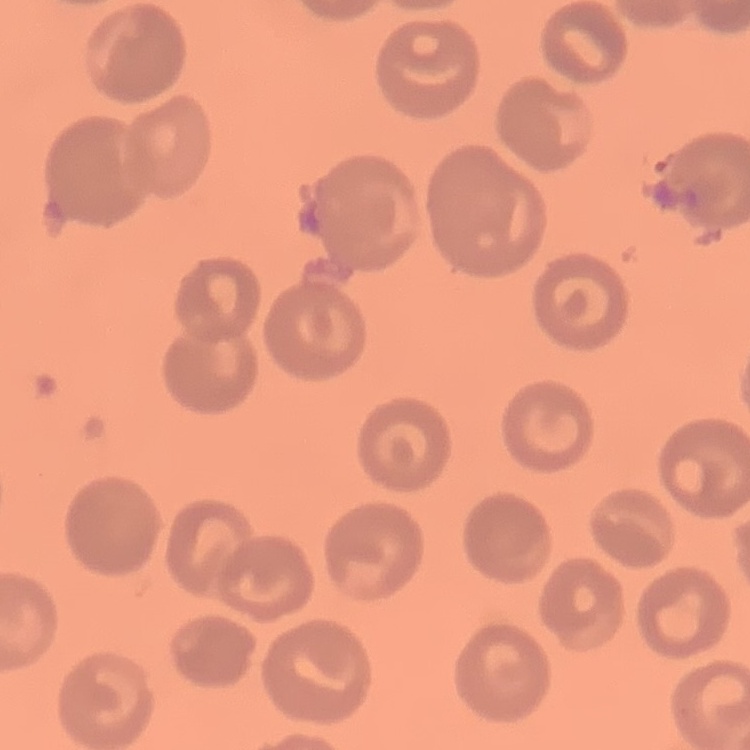
The erythrocytes show no rouleaux formation. Stained with either Field's or Giemsa. Thin blood film. Square crop of a larger photomicrograph.